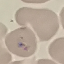

Result: negative for malaria parasites. Giemsa-stained preparation. Thin smear of blood. Cell patch, automatically extracted from a larger field of view and resized to 64 × 64 pixels. Photographed with a smartphone camera at the microscope eyepiece.